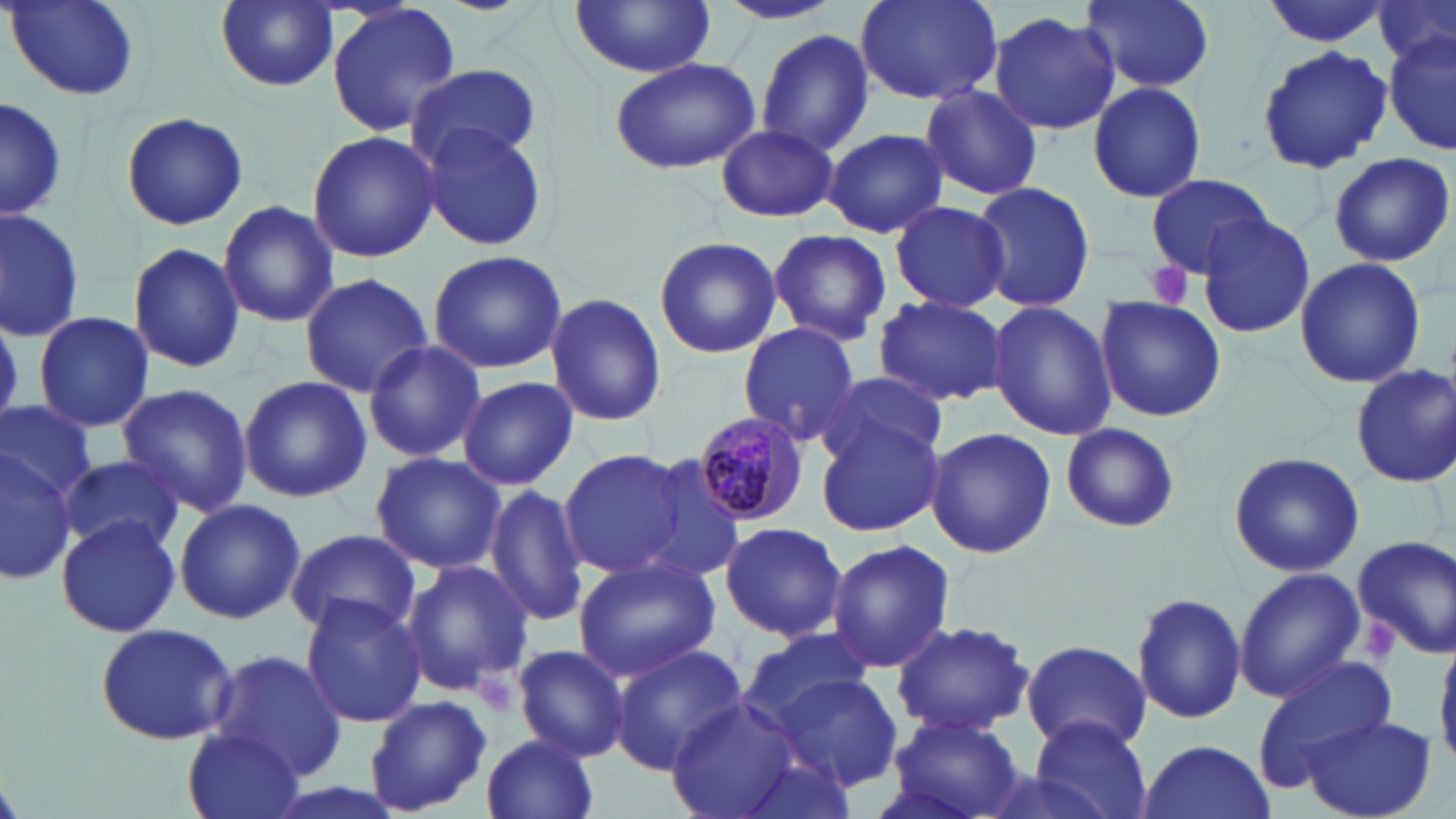

Summary:
  - Coordinate format: approximate bounding boxes as [x1, y1, x2, y2] in pixels
  - Plasmodium malariae-infected red blood cell locations: [696, 412, 810, 529]
  - Uninfected red blood cell locations: [215, 0, 337, 91], [855, 0, 1002, 106], [1084, 0, 1214, 91], [1261, 0, 1393, 48], [1376, 0, 1455, 73], [8, 1, 141, 104], [715, 1, 844, 26], [325, 2, 463, 140], [569, 2, 719, 78], [988, 11, 1121, 134], [755, 27, 877, 155], [1384, 31, 1456, 159], [1255, 44, 1392, 176], [607, 56, 761, 174], [409, 63, 543, 167], [1086, 80, 1209, 204], [919, 84, 1043, 201], [0, 96, 66, 225], [121, 111, 248, 230], [415, 120, 550, 253], [715, 124, 838, 222], [823, 128, 949, 238], [305, 130, 442, 263], [1326, 151, 1454, 267], [1145, 173, 1274, 279], [969, 179, 1096, 311], [890, 199, 1009, 312], [220, 200, 338, 327], [0, 205, 85, 341], [1196, 211, 1316, 340], [769, 229, 891, 345], [653, 237, 781, 358], [128, 241, 245, 373], [426, 250, 568, 374], [1293, 257, 1426, 390], [299, 274, 434, 396], [545, 293, 666, 428], [873, 294, 1008, 406], [1094, 299, 1226, 422], [985, 302, 1116, 439], [33, 311, 154, 433], [736, 323, 864, 446], [361, 340, 485, 462], [1349, 361, 1455, 485], [814, 373, 948, 472], [237, 375, 371, 503], [458, 376, 578, 491], [115, 384, 254, 516], [0, 399, 100, 504], [813, 412, 946, 535], [1059, 425, 1182, 534], [924, 427, 1057, 559], [0, 449, 77, 585], [557, 450, 693, 578], [371, 452, 505, 573], [1227, 452, 1365, 578], [59, 454, 184, 556], [629, 454, 746, 581], [484, 483, 590, 626], [174, 498, 305, 625], [55, 515, 182, 638], [718, 520, 847, 643], [287, 527, 420, 638], [1352, 535, 1456, 657], [827, 538, 955, 675], [572, 553, 723, 680], [400, 557, 534, 695], [1233, 567, 1367, 702], [1131, 591, 1247, 725], [299, 593, 426, 727], [891, 619, 1033, 737], [95, 622, 237, 746], [735, 628, 873, 727], [1435, 634, 1456, 770], [1017, 641, 1155, 753], [512, 644, 629, 761], [609, 644, 749, 773], [210, 649, 347, 780], [1251, 654, 1397, 785], [769, 671, 906, 791], [365, 696, 491, 816], [668, 698, 806, 819], [886, 709, 1026, 819], [1300, 715, 1437, 819], [1028, 717, 1153, 819], [184, 726, 306, 818], [481, 733, 601, 819], [1134, 738, 1276, 819], [729, 747, 862, 819]
  - Platelet locations: [1144, 261, 1197, 309], [1363, 620, 1403, 666], [474, 673, 520, 717]
  - Slide-level diagnosis: Plasmodium malariae
  - Field of view: single
  - Modality: light microscopy
  - Magnification: 1000x
  - Preparation: thin blood smear
  - Stain: May-Grünwald-Giemsa
  - Image size: 1456×819 pixels